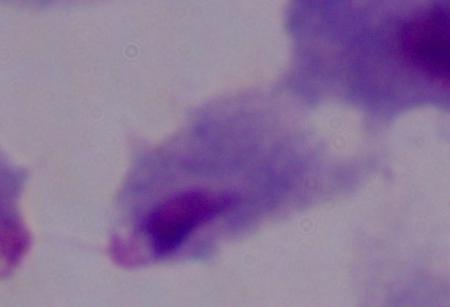
Summary:
  - Magnification: 1000x
  - Identification: trichomonad
  - Modality: micrograph